Describe the morphology of the red blood cells.
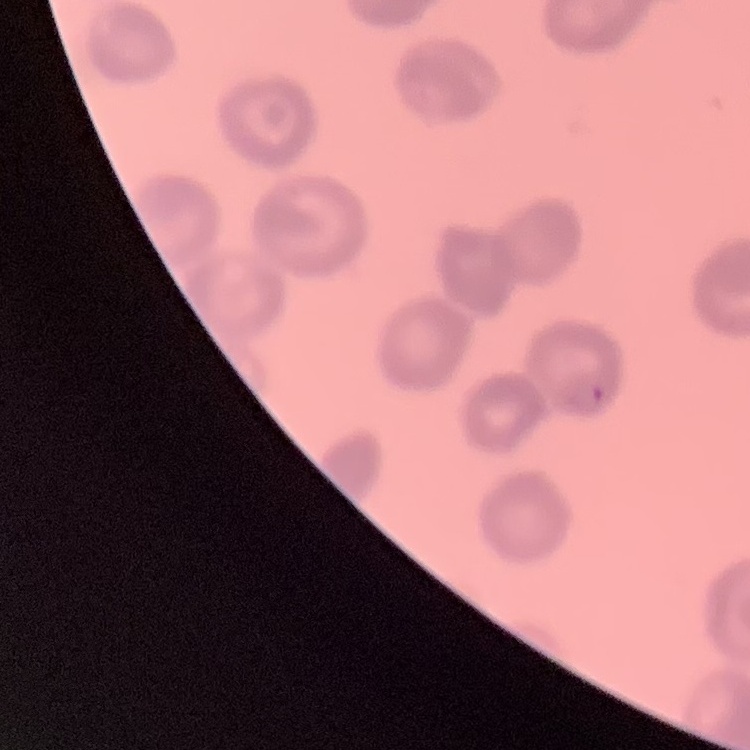
They show rouleaux formation.

stain = Field's or Giemsa
preparation = thin blood smear
image type = one tile cut from a larger photomicrograph